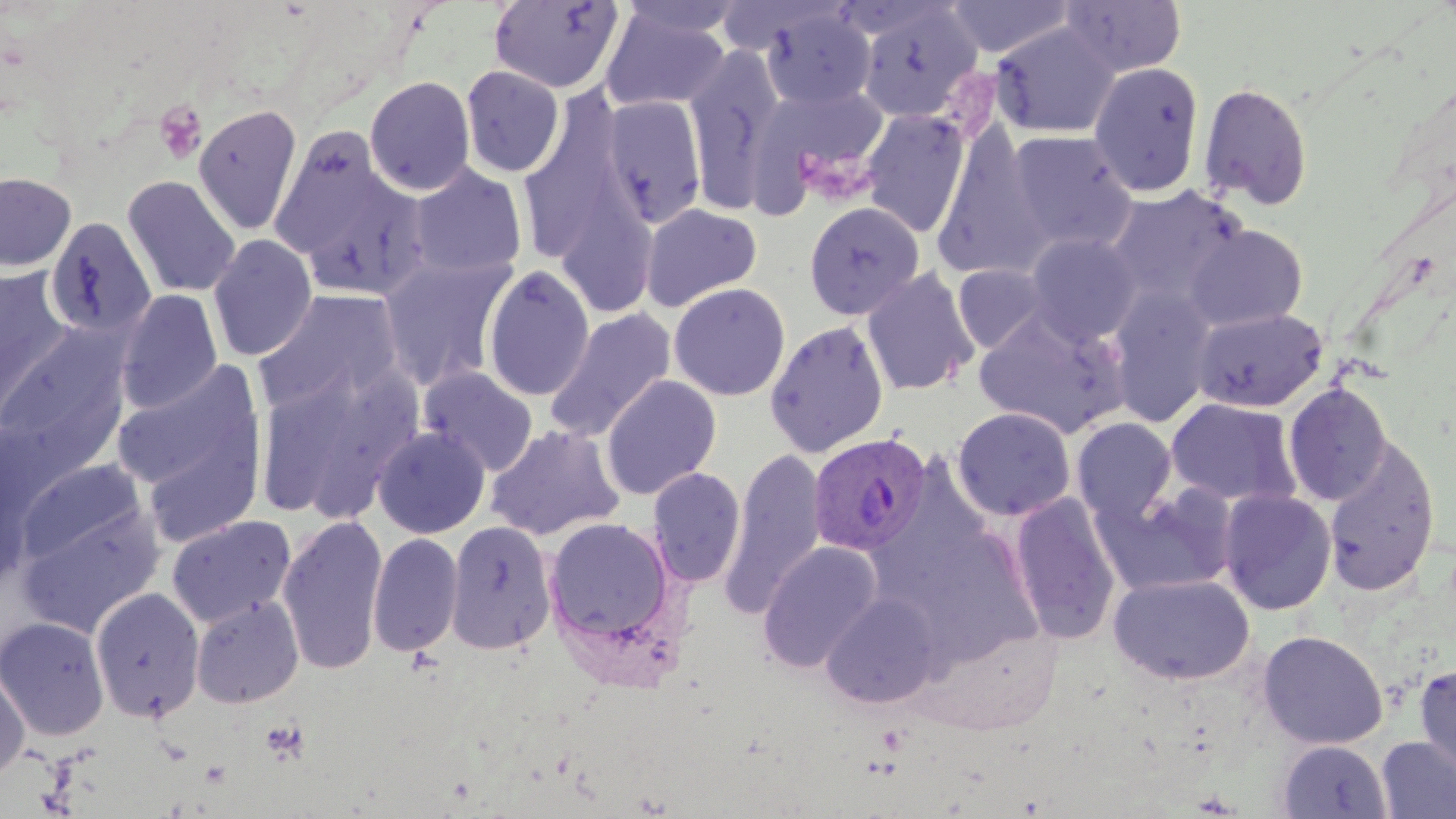 Approximate bounding boxes as (x1,y1)-(x2,y2) corner pairs in pixels. Uninfected red blood cell locations: (489,0)-(626,94), (615,0)-(751,40), (945,0)-(1076,59), (1060,0)-(1187,78), (855,4)-(984,125), (599,6)-(730,113), (760,7)-(876,112), (991,22)-(1119,139), (685,45)-(783,216), (1088,62)-(1205,197), (459,65)-(565,177), (364,75)-(476,196), (1199,82)-(1313,210), (749,86)-(890,210), (601,96)-(707,229), (518,98)-(629,268), (192,103)-(304,236), (861,109)-(970,238), (933,127)-(1051,282), (268,128)-(406,269), (1007,130)-(1138,254), (409,164)-(527,279), (0,171)-(76,272), (122,175)-(241,298), (1106,184)-(1248,307), (804,201)-(924,321), (640,202)-(763,312), (42,219)-(162,343), (1185,224)-(1308,331), (208,234)-(317,361), (1026,234)-(1141,345), (379,255)-(517,392), (952,264)-(1050,354), (483,265)-(595,401), (0,266)-(73,419), (862,267)-(979,396), (961,271)-(1109,396), (668,282)-(791,401), (1107,288)-(1216,427), (116,289)-(222,414), (254,289)-(405,415), (1193,307)-(1327,412), (544,308)-(677,442), (974,310)-(1127,438), (766,319)-(889,458), (0,329)-(133,470), (111,360)-(264,501), (256,360)-(422,523), (418,367)-(538,476), (600,375)-(722,500), (1283,382)-(1393,506), (1165,398)-(1301,507), (952,407)-(1075,521), (1071,417)-(1177,523), (486,424)-(624,541), (372,426)-(490,538), (1323,435)-(1440,598), (720,447)-(827,618), (16,457)-(147,568), (648,466)-(747,588), (1094,481)-(1239,596), (1218,489)-(1337,615), (1008,492)-(1121,644), (17,500)-(165,638), (276,513)-(388,677), (166,514)-(296,628), (543,517)-(677,650), (446,519)-(557,654), (367,532)-(463,657), (757,540)-(883,673), (1108,573)-(1255,685), (90,586)-(205,723), (821,592)-(943,709), (191,595)-(304,708), (0,616)-(110,741), (1257,629)-(1389,749), (1413,663)-(1456,781), (0,664)-(30,783), (1376,735)-(1456,818), (1277,739)-(1392,818). Plasmodium vivax-infected red blood cell locations: (808,433)-(931,556). Platelet locations: (153,100)-(208,164), (262,719)-(309,763). Slide-level diagnosis: Plasmodium vivax. One field of a larger specimen. 1000x magnification. Image is 1456×819 pixels. Thin blood smear. Light microscopy. May-Grünwald-Giemsa-stained preparation.